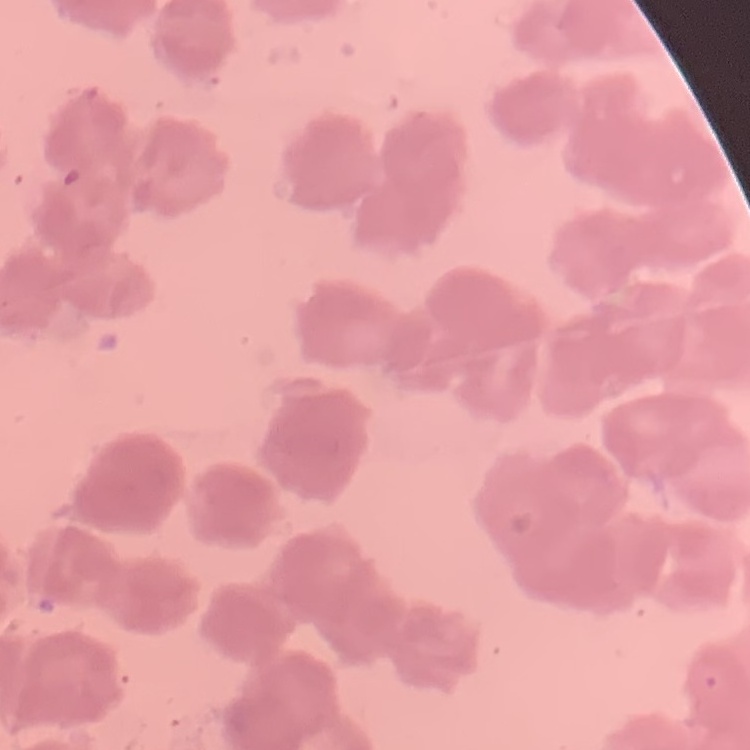

Summary:
  - Red blood cell morphology: rouleaux formation
  - Preparation: thin peripheral smear
  - Stain: Field's or Giemsa
  - Image type: one tile cut from a larger photomicrograph